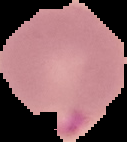
Image is 127×142 pixels. Malaria status: parasitized. The area outside the segmented cell region is set to black. From a thin blood smear.